Describe the morphology of the erythrocytes.
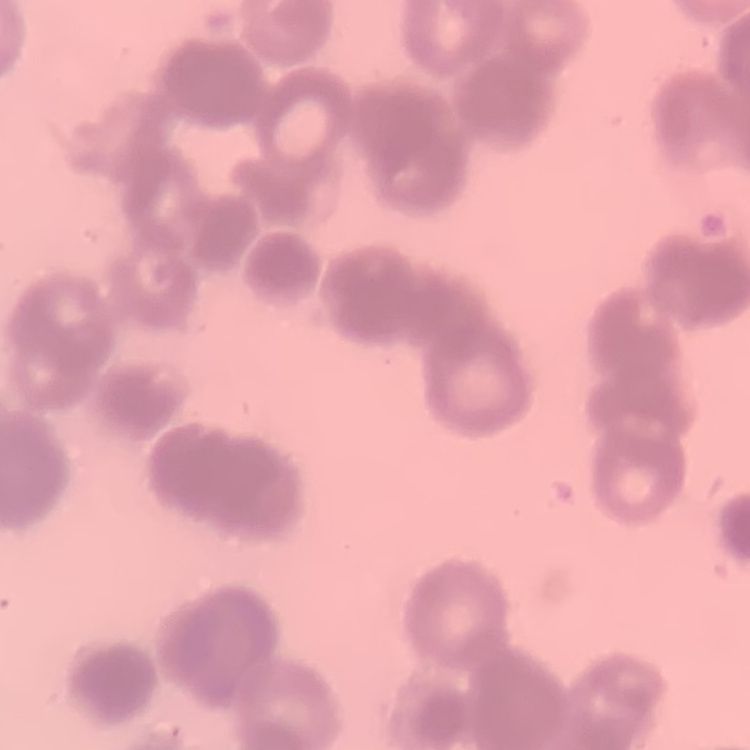

Rouleaux formation.

stain = Field's or Giemsa
preparation = thin peripheral smear
image type = square crop of a larger photomicrograph